Report the malaria status of this cell.
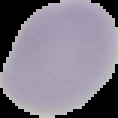

Uninfected.

Cell region segmented out of the field of view; the surrounding area is masked to black. Image is 118×118 pixels. From a thin blood film.